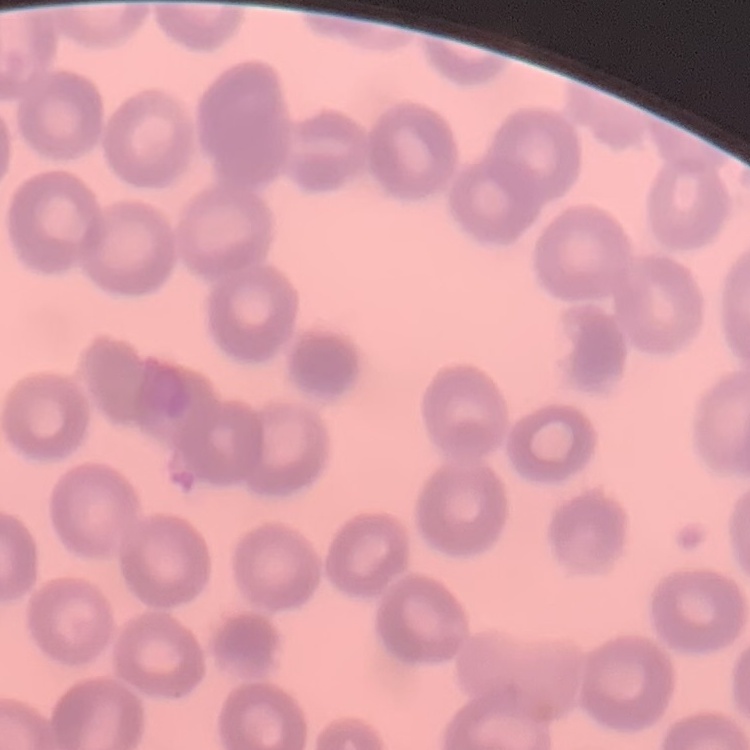

The red blood cells exhibit no rouleaux formation. Field's or Giemsa stain. Thin peripheral smear. Square crop of a larger photomicrograph.